Locate and identify every blood parasite.
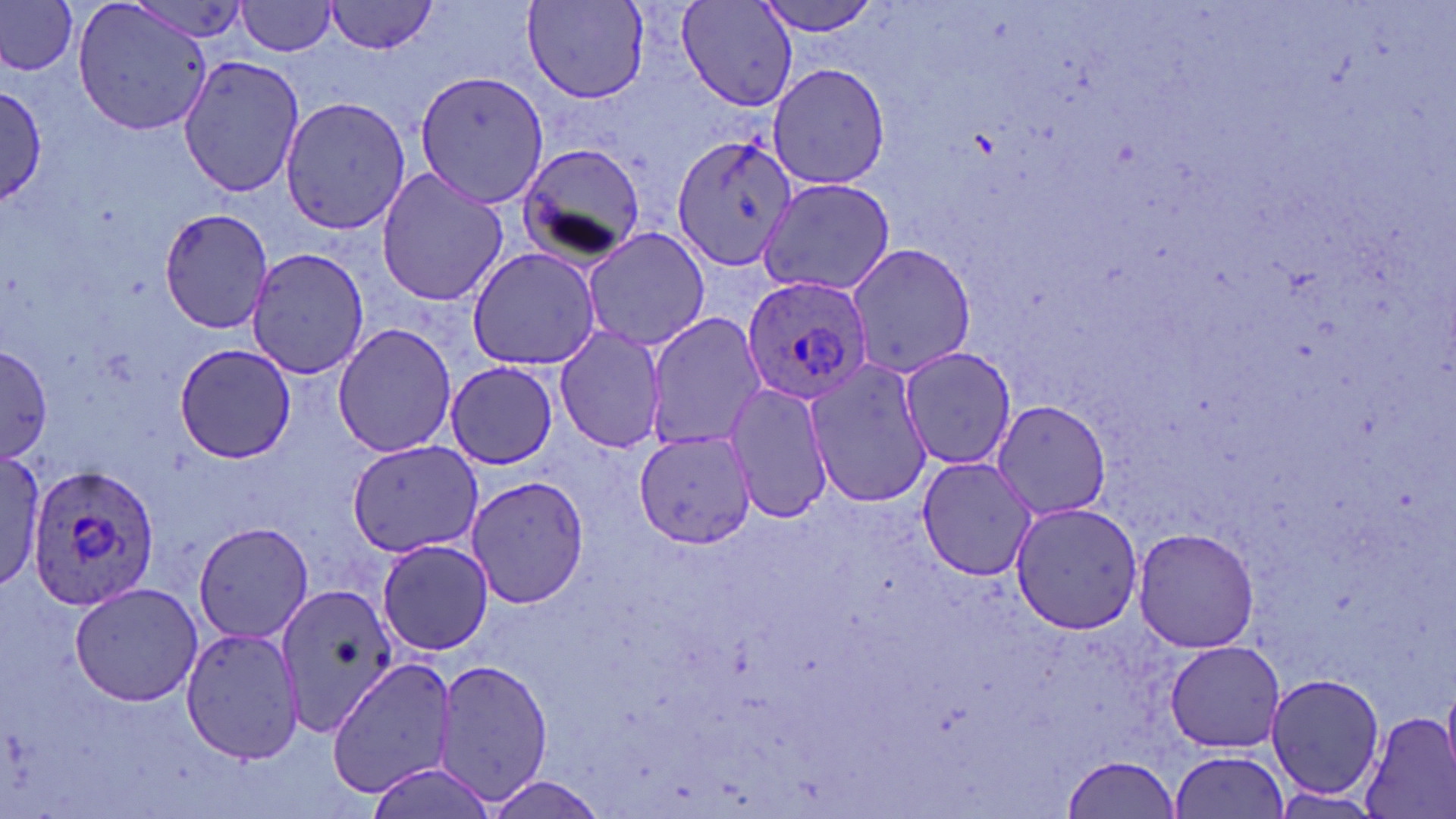
Approximate bounding boxes as (x1, y1, x2, y2) in pixels.
Plasmodium ovale-infected red blood cells: (740, 271, 874, 405), (27, 458, 164, 610).
No Plasmodium falciparum, Plasmodium malariae, Plasmodium vivax, Babesia divergens, or Trypanosoma brucei observed.

Summary:
  - Uninfected red blood cell locations: (69, 0, 215, 137), (238, 0, 338, 56), (326, 0, 440, 55), (755, 0, 885, 39), (521, 1, 650, 104), (0, 2, 81, 75), (677, 2, 797, 110), (177, 55, 305, 198), (767, 63, 890, 191), (417, 71, 550, 210), (1, 84, 47, 204), (280, 96, 411, 235), (673, 133, 801, 273), (513, 142, 647, 264), (376, 167, 511, 308), (759, 177, 895, 299), (159, 207, 274, 334), (582, 226, 710, 353), (844, 241, 976, 378), (242, 247, 371, 380), (467, 247, 600, 371), (645, 312, 767, 453), (332, 321, 456, 459), (554, 322, 666, 455), (172, 342, 297, 464), (0, 347, 53, 463), (898, 347, 1017, 470), (804, 356, 930, 509), (446, 361, 562, 468), (725, 382, 834, 526), (988, 398, 1111, 521), (632, 432, 758, 549), (347, 439, 483, 557), (0, 448, 48, 593), (915, 456, 1035, 581), (467, 473, 590, 609), (1007, 498, 1146, 634), (192, 522, 313, 644), (1134, 528, 1259, 653), (376, 539, 495, 655), (69, 580, 206, 706), (278, 584, 399, 735), (179, 625, 304, 767), (1164, 640, 1284, 753), (436, 657, 554, 805), (326, 659, 457, 797), (1267, 672, 1386, 801), (1359, 711, 1456, 819), (1170, 751, 1289, 818), (1061, 754, 1180, 818), (364, 762, 499, 819), (481, 777, 610, 818)
  - Slide-level diagnosis: Plasmodium ovale
  - Stain: May-Grünwald-Giemsa
  - Modality: optical microscopy
  - Field of view: single
  - Image size: 1456×819 pixels
  - Magnification: 1000x
  - Preparation: thin blood smear